Identify the preparation type.
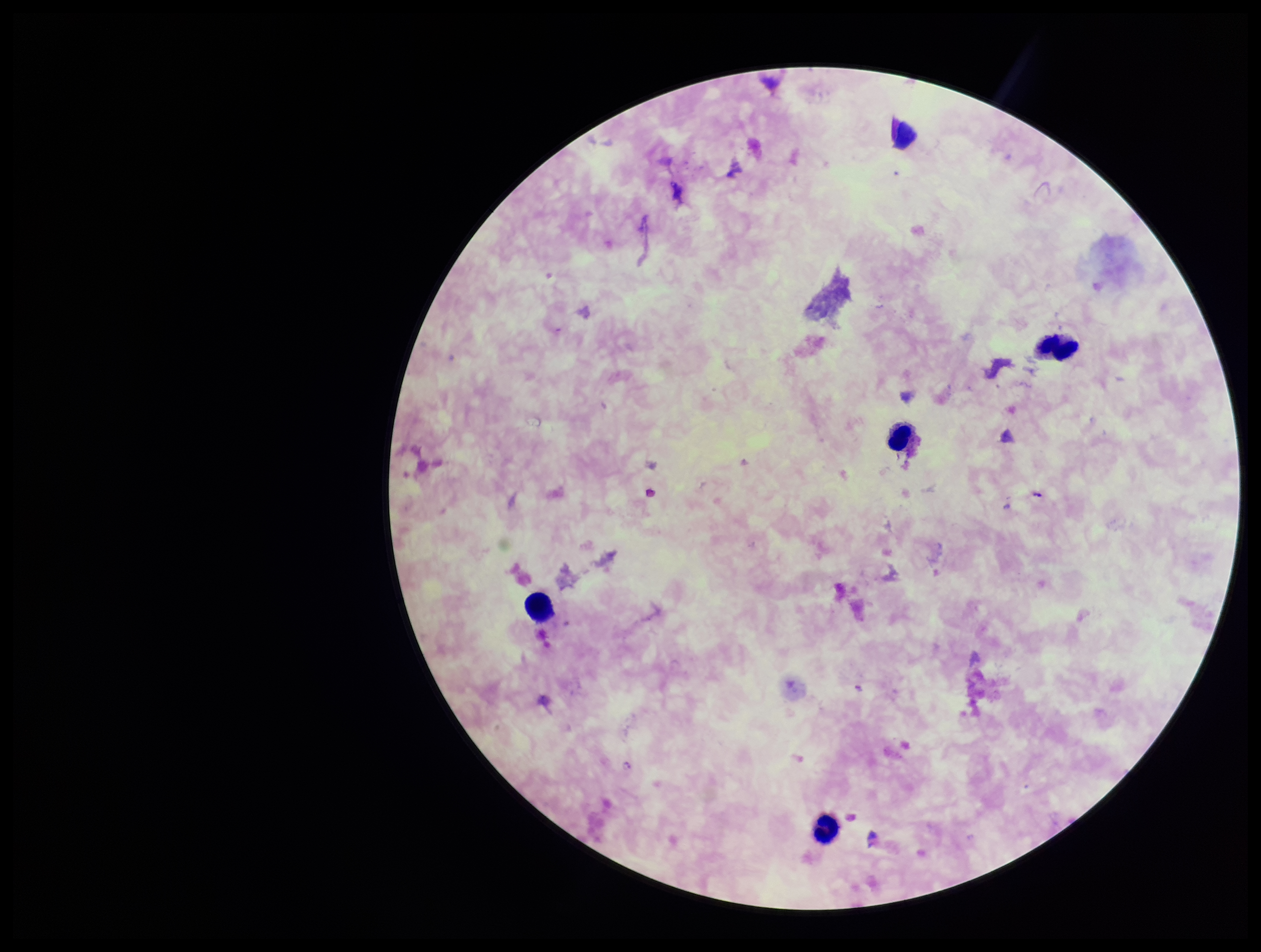
It is a thick blood smear.

Single field of view. Parasite count: 1. Photographed through the microscope eyepiece with a smartphone camera. Plasmodium parasites: identified. Leukocyte count: 5. Patient malaria status: infected. Species reported for this patient: Plasmodium falciparum. Image is 1261×952 pixels. Stained with Giemsa.